Evaluate for malaria.
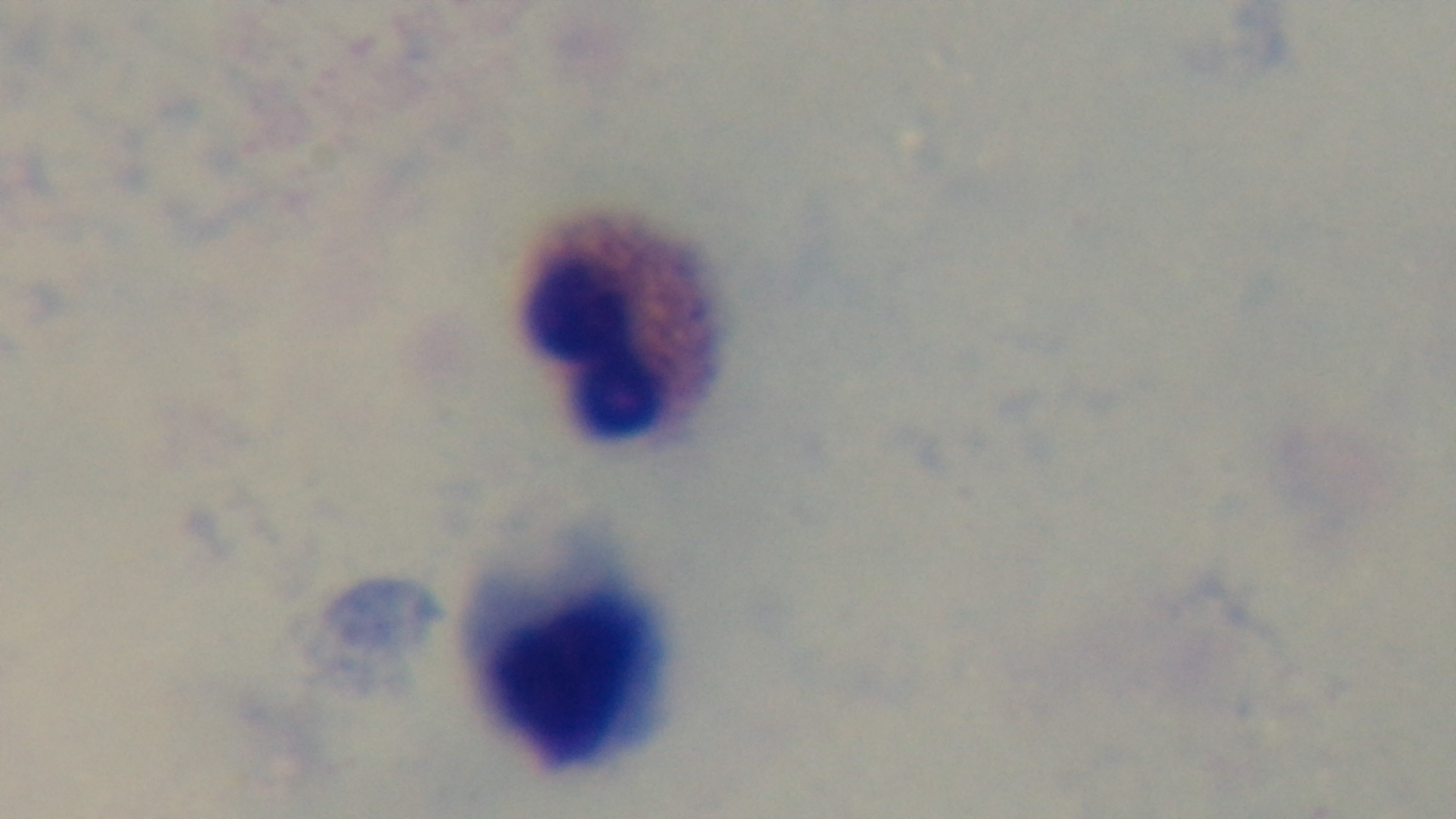

It is uninfected.

Summary:
  - Preparation: thick smear
  - Stain: Giemsa
  - Objective: 100x oil immersion
  - Modality: light microscopy
  - Field of view: single
  - Capture: mounted 4K digital camera